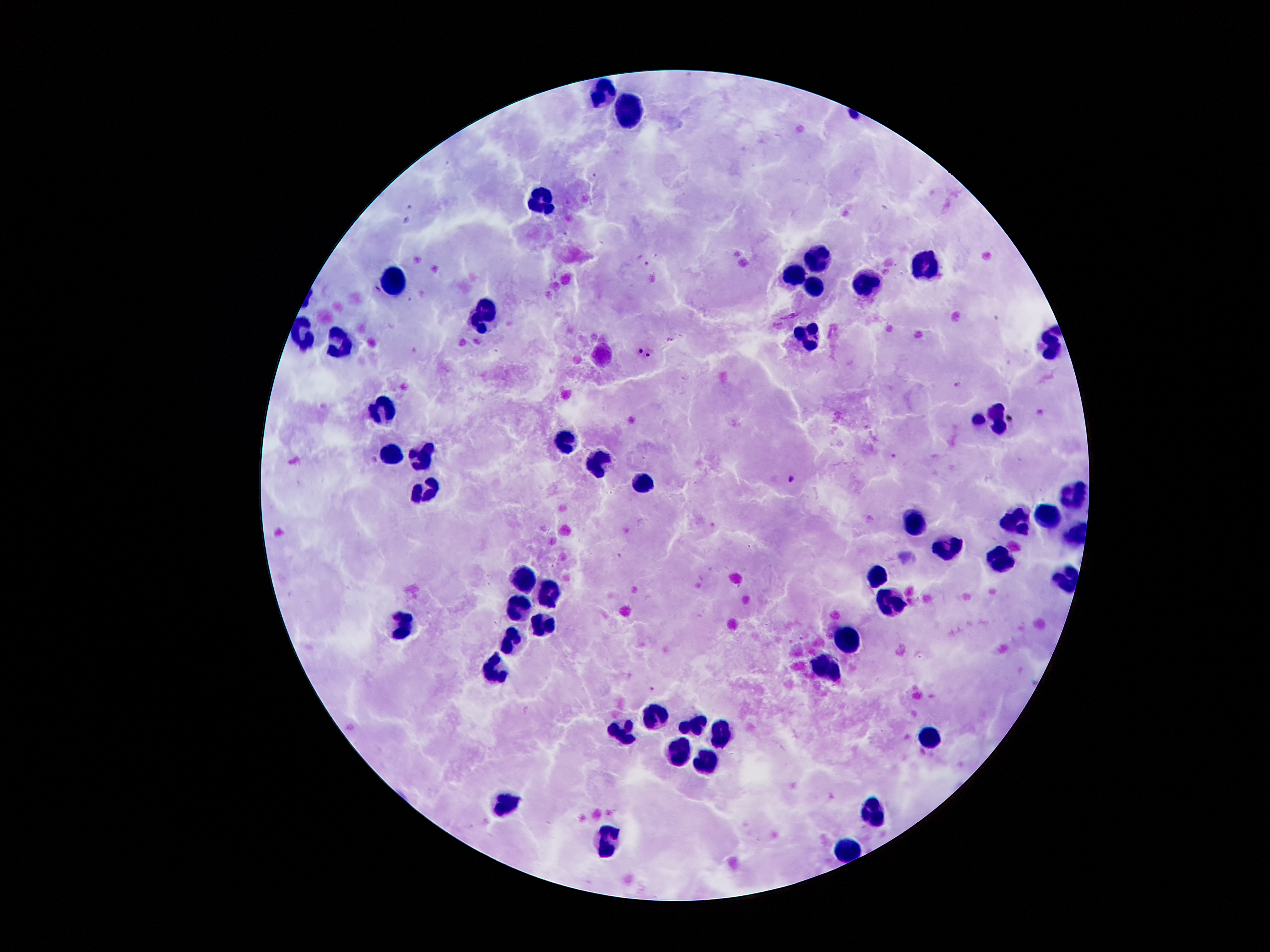

Approximate object centers, in pixels from the top-left corner.
Summary:
  - Leukocyte locations: (x=599, y=91), (x=631, y=112), (x=541, y=208), (x=819, y=258), (x=921, y=270), (x=794, y=276), (x=813, y=281), (x=392, y=284), (x=866, y=284), (x=481, y=312), (x=300, y=334), (x=806, y=339), (x=1048, y=342), (x=344, y=345), (x=384, y=413), (x=991, y=417), (x=567, y=439), (x=423, y=452), (x=392, y=455), (x=601, y=463), (x=639, y=479), (x=426, y=486), (x=1072, y=491), (x=1046, y=517), (x=1016, y=521), (x=910, y=525), (x=946, y=549), (x=1001, y=558), (x=524, y=578), (x=876, y=579), (x=549, y=590), (x=893, y=605), (x=517, y=606), (x=400, y=623), (x=544, y=623), (x=844, y=638), (x=515, y=640), (x=827, y=664), (x=497, y=667), (x=654, y=710), (x=699, y=724), (x=624, y=729), (x=719, y=730), (x=927, y=736), (x=679, y=752), (x=706, y=762), (x=507, y=800), (x=875, y=809), (x=607, y=836), (x=848, y=848)
  - Plasmodium parasite locations: (x=648, y=263), (x=639, y=349), (x=649, y=353), (x=959, y=384), (x=789, y=478)
  - Field of view: single
  - Image size: 1270×952 pixels
  - Preparation: thick blood smear
  - Magnification: 100x
  - Patient malaria status: infected with Plasmodium falciparum
  - Capture: smartphone through the microscope eyepiece
  - Stain: Giemsa